State the blood parasite species.
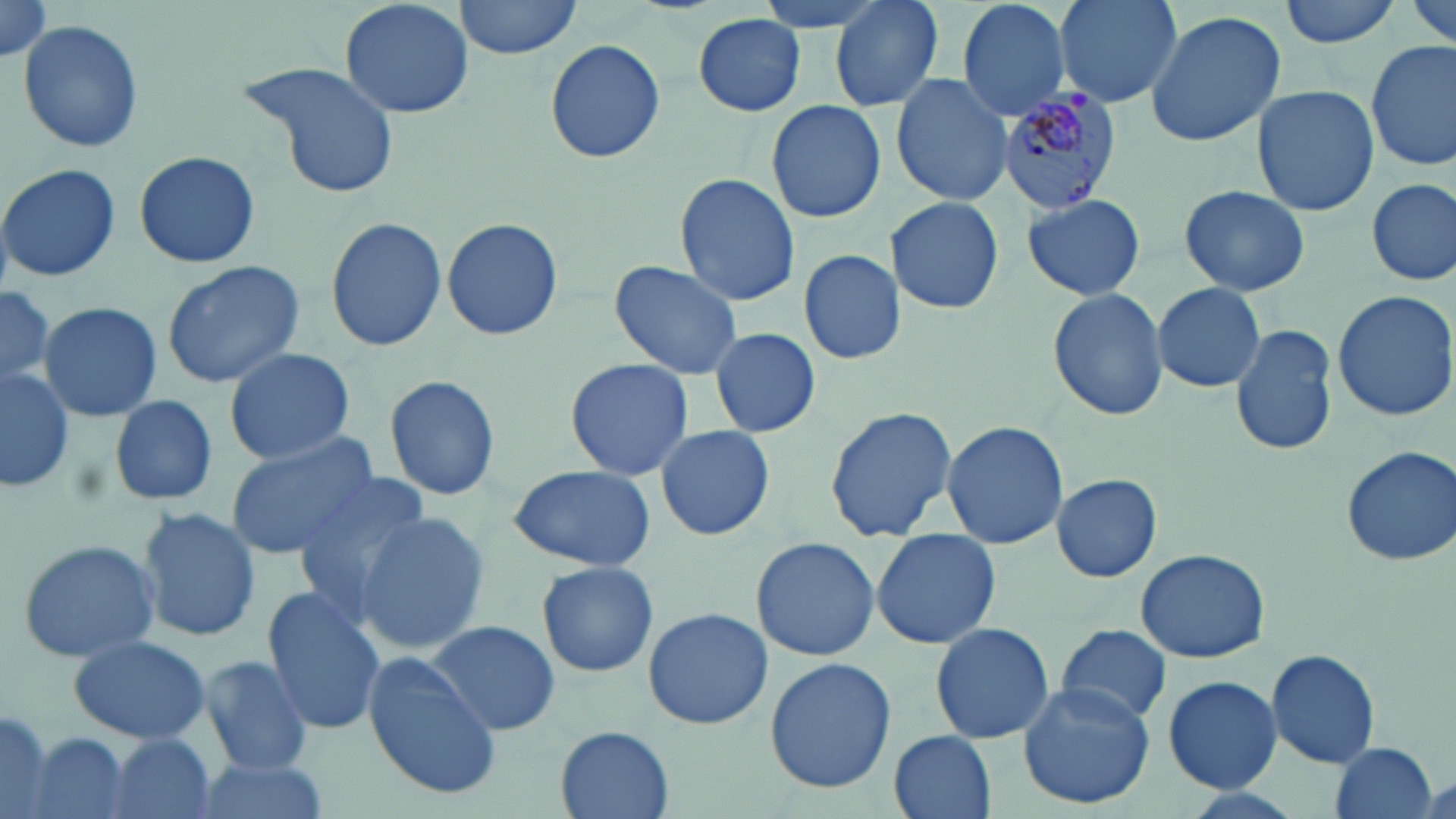
Plasmodium malariae.

image size = 1456×819 pixels
uninfected red blood cell locations = approximate bounding boxes as (x1, y1, x2, y2) in pixels: (337, 0, 475, 120), (454, 0, 584, 57), (750, 0, 894, 35), (829, 0, 947, 114), (955, 0, 1072, 122), (1054, 0, 1185, 110), (1278, 0, 1402, 49), (1404, 0, 1455, 54), (0, 3, 54, 66), (1142, 10, 1286, 147), (694, 13, 806, 116), (17, 19, 145, 156), (545, 38, 666, 165), (1366, 40, 1455, 173), (238, 60, 403, 199), (891, 72, 1015, 207), (1250, 85, 1379, 216), (766, 100, 886, 224), (133, 150, 260, 269), (0, 163, 120, 283), (673, 172, 802, 306), (1367, 177, 1454, 288), (1176, 184, 1311, 297), (1020, 192, 1147, 301), (887, 195, 1004, 314), (325, 214, 447, 352), (442, 215, 562, 342), (794, 250, 904, 365), (608, 259, 743, 380), (160, 260, 304, 389), (1152, 282, 1267, 392), (0, 285, 65, 403), (1048, 286, 1170, 420), (1331, 288, 1456, 422), (37, 300, 161, 424), (1230, 322, 1341, 458), (709, 327, 823, 438), (224, 348, 355, 464), (564, 358, 697, 481), (0, 363, 73, 495), (384, 375, 502, 501), (110, 395, 218, 505), (824, 405, 958, 542), (942, 420, 1068, 548), (656, 425, 774, 541), (222, 434, 379, 560), (1340, 445, 1456, 567), (504, 465, 658, 570), (286, 472, 433, 616), (1050, 472, 1164, 582), (136, 507, 261, 644), (353, 513, 490, 653), (871, 528, 1000, 649), (751, 536, 880, 660), (16, 537, 162, 663), (1136, 547, 1271, 663), (535, 560, 659, 678), (261, 587, 386, 736), (642, 606, 772, 730), (427, 620, 562, 739), (931, 622, 1054, 746), (1055, 623, 1173, 727), (66, 633, 215, 745), (1264, 648, 1383, 769), (362, 654, 499, 799), (199, 656, 314, 775), (765, 656, 896, 793), (1162, 675, 1282, 792), (1016, 681, 1155, 810), (0, 704, 54, 818), (555, 726, 674, 819), (889, 731, 998, 819), (21, 733, 140, 819), (105, 735, 218, 819), (1327, 741, 1439, 819), (190, 756, 331, 819)
modality = light microscopy
preparation = thin blood smear
magnification = 1000x
Plasmodium malariae-infected red blood cell locations = approximate bounding boxes as (x1, y1, x2, y2) in pixels: (993, 89, 1123, 214)
stain = May-Grünwald-Giemsa
field of view = one of a larger specimen